Report the malaria status of this cell.
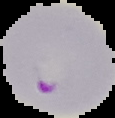

It is parasitized.

Cell region segmented out of the field of view; the surrounding area is masked to black. Image is 115×118 pixels. From a thin blood smear.